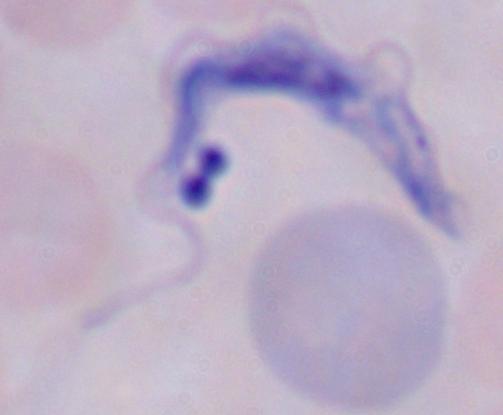

magnification: 1000x
identification: trypanosome
modality: micrograph